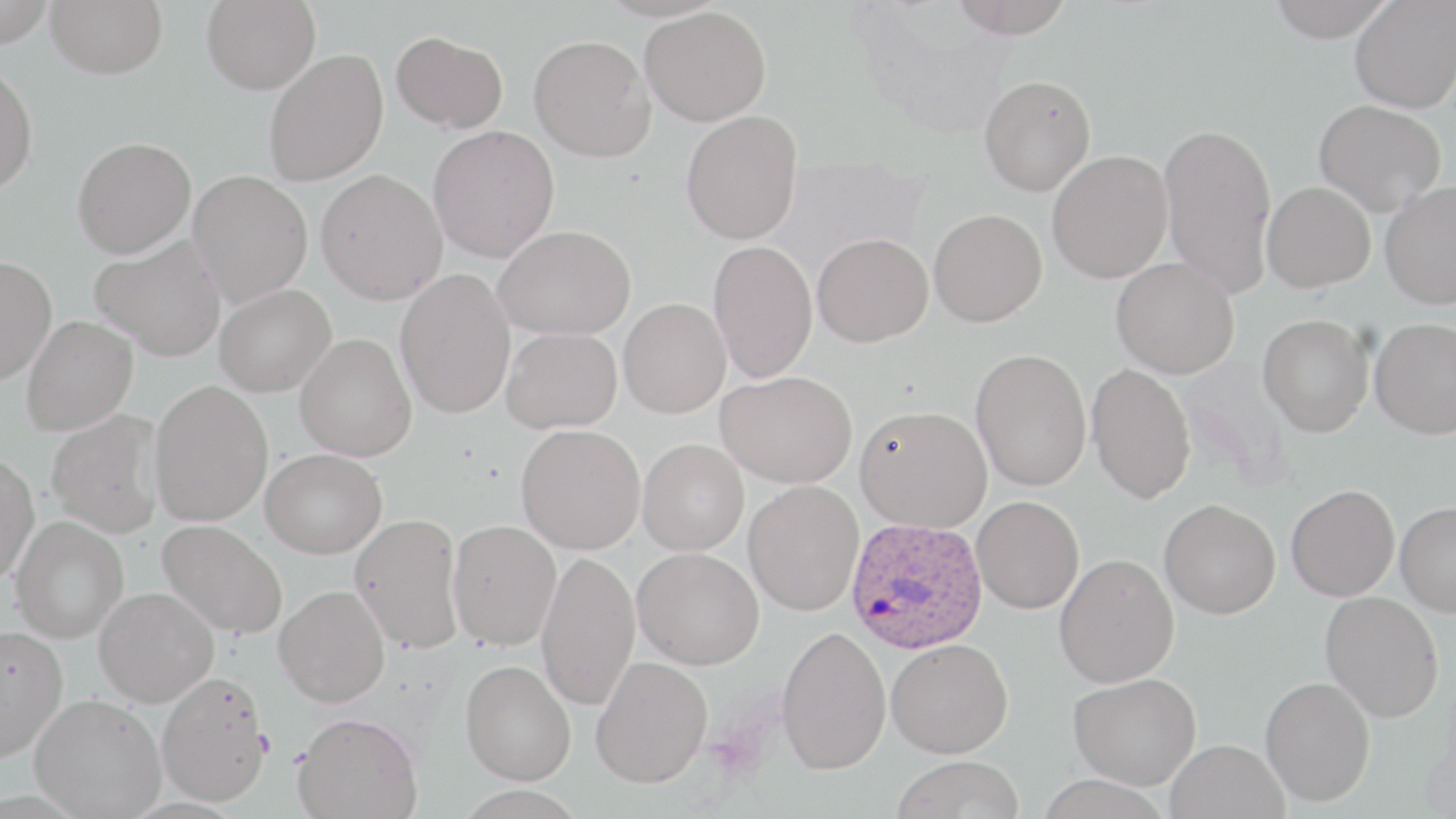
Summary:
  - Coordinate format: approximate bounding boxes as (x1, y1, x2, y2) in pixels
  - Uninfected red blood cell locations: (0, 0, 57, 47), (46, 0, 168, 78), (201, 0, 321, 95), (947, 0, 1078, 39), (1266, 0, 1398, 42), (1350, 0, 1456, 113), (640, 6, 771, 126), (391, 31, 508, 133), (529, 34, 655, 162), (263, 49, 389, 186), (0, 63, 39, 196), (978, 74, 1096, 196), (1314, 100, 1446, 215), (680, 109, 803, 245), (1158, 121, 1277, 298), (428, 125, 560, 263), (72, 137, 197, 257), (1047, 150, 1173, 283), (315, 169, 447, 304), (187, 170, 313, 307), (1261, 181, 1375, 293), (1380, 181, 1456, 309), (928, 208, 1047, 327), (493, 224, 636, 339), (812, 232, 933, 346), (89, 234, 228, 361), (708, 239, 818, 383), (0, 255, 57, 385), (1111, 256, 1239, 378), (395, 269, 516, 419), (214, 283, 336, 397), (619, 298, 731, 418), (1258, 314, 1374, 436), (21, 316, 138, 436), (1370, 317, 1456, 439), (501, 326, 623, 433), (295, 332, 417, 461), (970, 348, 1092, 491), (1088, 363, 1196, 504), (716, 370, 857, 488), (149, 380, 273, 525), (855, 405, 991, 532), (46, 409, 165, 538), (516, 424, 646, 554), (637, 437, 750, 555), (261, 448, 386, 558), (0, 452, 39, 583), (743, 480, 864, 616), (1286, 484, 1399, 601), (972, 496, 1084, 614), (1159, 498, 1280, 618), (1395, 501, 1456, 617), (349, 512, 464, 653), (9, 515, 129, 642), (157, 519, 287, 639), (447, 519, 561, 650), (632, 546, 764, 669), (535, 551, 641, 711), (1054, 553, 1179, 687), (274, 585, 390, 706), (94, 586, 219, 706), (1320, 590, 1444, 722), (776, 625, 891, 774), (0, 626, 67, 760), (886, 637, 1013, 757), (591, 655, 713, 788), (460, 660, 576, 784), (1068, 671, 1201, 789), (156, 672, 271, 806), (1260, 676, 1375, 806), (30, 693, 166, 818), (293, 711, 422, 819), (1165, 739, 1289, 819), (892, 755, 1024, 818)
  - Plasmodium ovale-infected red blood cell locations: (845, 516, 989, 654)
  - Platelet locations: (253, 730, 276, 758)
  - Slide-level diagnosis: Plasmodium ovale
  - Stain: May-Grünwald-Giemsa
  - Magnification: 1000x
  - Preparation: thin blood smear
  - Field of view: single
  - Modality: light microscopy
  - Image size: 1456×819 pixels